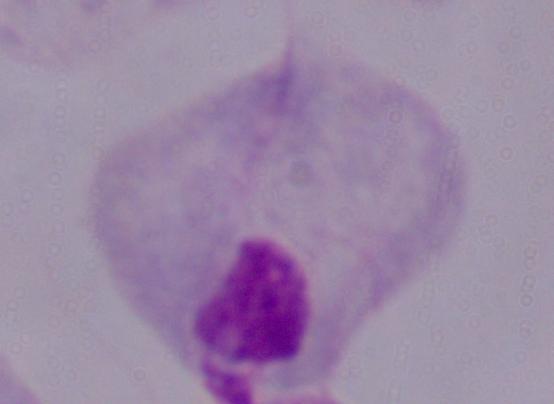 Captured at 1000x magnification. Photomicrograph. A trichomonad is shown.